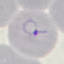
result: malaria parasites identified
image_type: automatically extracted cell patch, resized to 64 × 64 pixels
stain: Giemsa
capture: smartphone through the microscope eyepiece
preparation: thin blood film